Report the malaria status of this cell.
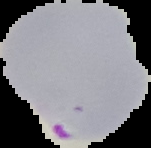
It is parasitized.

Summary:
  - Preparation: thin blood smear
  - Image type: cell region segmented out of the field of view; surrounding area masked to black
  - Image size: 151×148 pixels